Identify the preparation type.
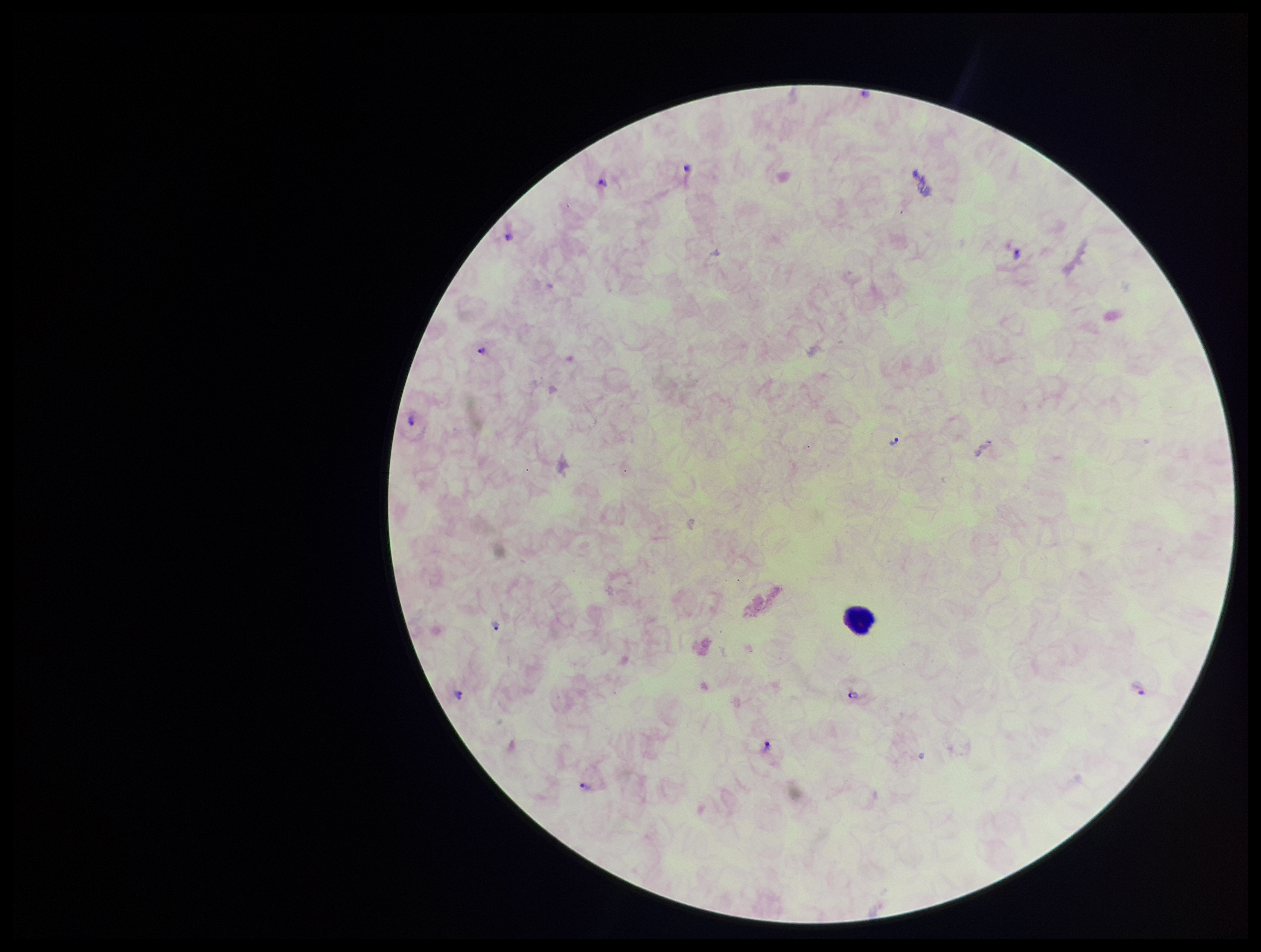
It is a thick blood smear.

species reported for this patient = Plasmodium vivax
Plasmodium parasites = detected
field of view = single
parasite count = 11
capture = smartphone photograph through the microscope eyepiece
leukocyte count = 1
patient malaria status = infected
stain = Giemsa
image size = 1261×952 pixels